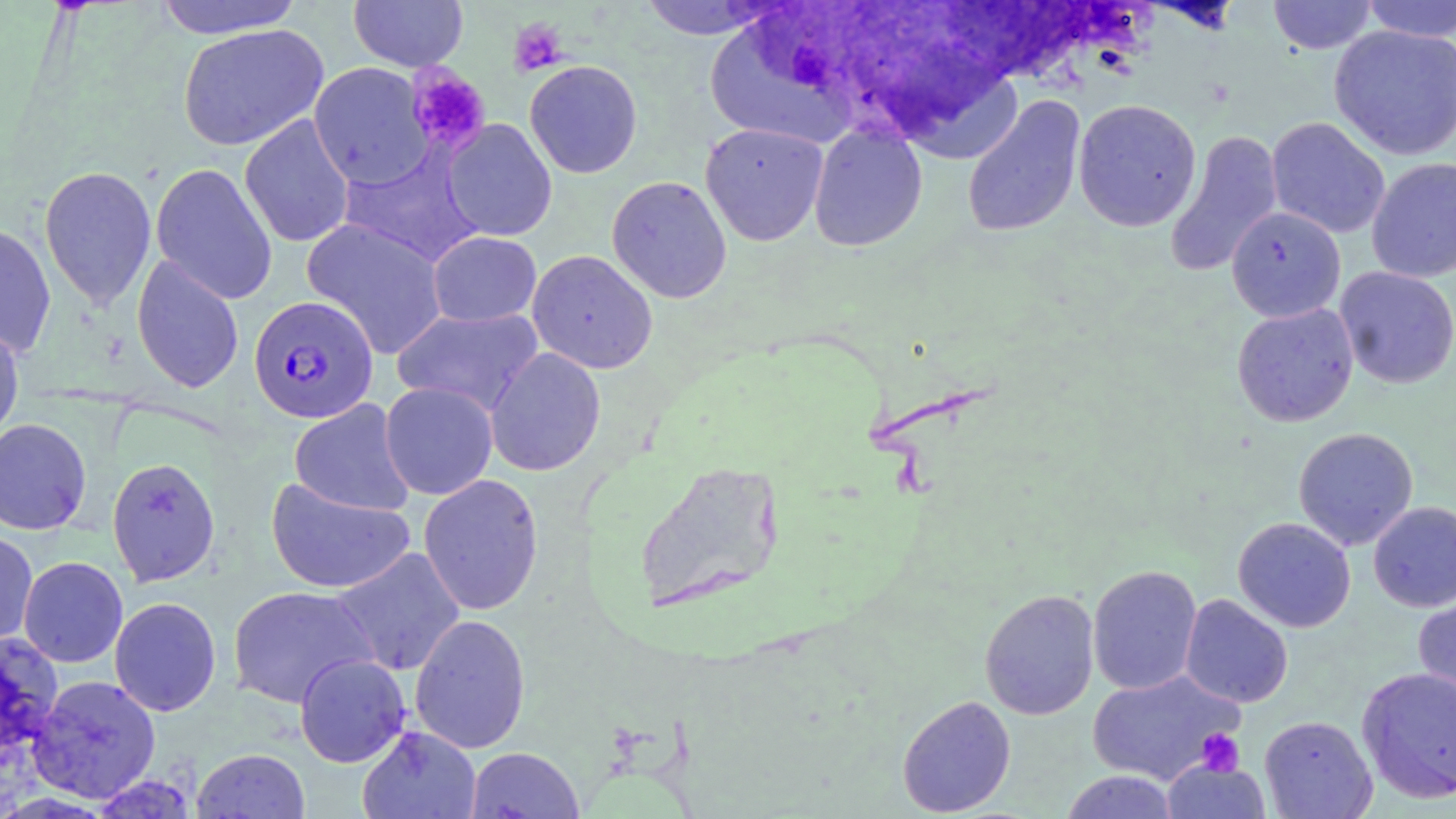

Summary:
  - Coordinate format: approximate bounding boxes as (x1, y1, x2, y2) in pixels
  - Plasmodium falciparum-infected red blood cell locations: (248, 294, 379, 423)
  - Platelet locations: (508, 17, 569, 76), (405, 64, 491, 154), (1196, 729, 1245, 776)
  - Uninfected red blood cell locations: (152, 0, 306, 39), (348, 0, 468, 72), (1268, 0, 1377, 54), (1359, 0, 1456, 42), (637, 1, 785, 40), (178, 24, 329, 151), (1329, 25, 1456, 160), (701, 26, 869, 148), (886, 58, 1027, 166), (524, 60, 643, 179), (308, 62, 434, 189), (961, 95, 1087, 238), (1073, 99, 1202, 232), (239, 115, 355, 248), (1266, 117, 1390, 239), (442, 119, 557, 241), (700, 122, 828, 246), (808, 122, 927, 252), (1164, 130, 1284, 278), (338, 147, 483, 267), (1366, 157, 1456, 283), (150, 162, 277, 305), (39, 165, 157, 311), (606, 175, 732, 303), (1226, 206, 1346, 322), (301, 217, 448, 359), (0, 223, 57, 358), (428, 232, 542, 327), (527, 249, 658, 374), (131, 255, 244, 394), (1334, 266, 1456, 388), (1231, 303, 1359, 427), (391, 307, 544, 417), (0, 319, 25, 446), (484, 347, 606, 477), (380, 381, 498, 500), (288, 400, 416, 516), (0, 419, 92, 535), (1293, 427, 1419, 550), (107, 457, 221, 587), (633, 460, 787, 614), (418, 473, 544, 616), (265, 476, 416, 594), (1368, 501, 1456, 612), (1233, 517, 1356, 632), (0, 530, 38, 647), (330, 547, 466, 676), (18, 556, 128, 668), (1087, 564, 1202, 695), (227, 585, 378, 708), (1413, 586, 1456, 711), (979, 589, 1100, 720), (1180, 594, 1293, 708), (109, 596, 222, 717), (409, 614, 531, 754), (0, 632, 64, 757), (294, 653, 412, 768), (1356, 666, 1456, 803), (1087, 669, 1244, 784), (27, 675, 161, 804), (897, 695, 1016, 816), (1259, 715, 1378, 818), (358, 725, 481, 819), (466, 747, 585, 818), (192, 748, 310, 818), (1162, 760, 1271, 819), (1060, 770, 1181, 819)
  - Slide-level diagnosis: Plasmodium falciparum
  - Image size: 1456×819 pixels
  - Stain: May-Grünwald-Giemsa
  - Modality: optical microscopy
  - Magnification: 1000x
  - Preparation: thin blood smear
  - Field of view: one of a larger specimen